Point out each malaria parasite.
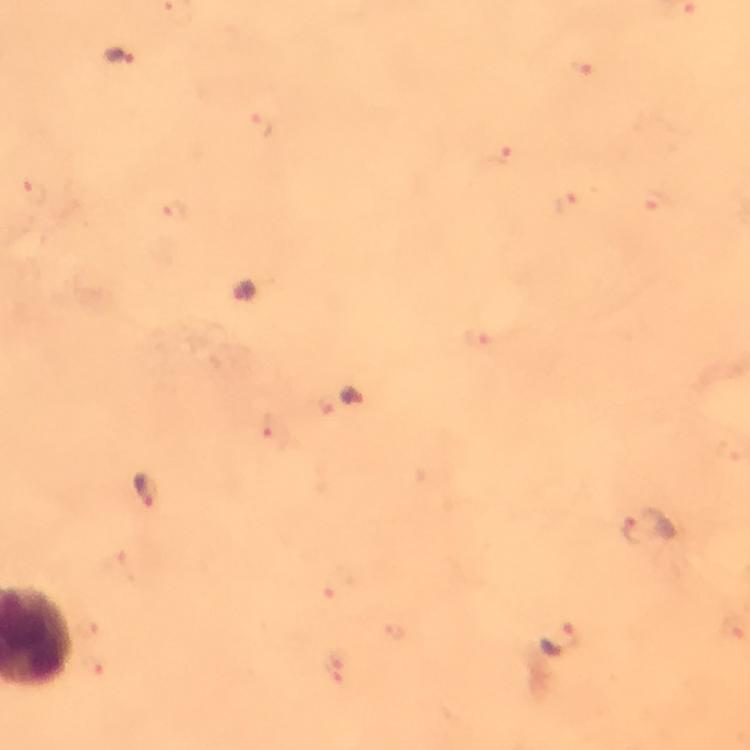

Approximate centers as (x, y) in pixels.
Malaria parasites: (119, 56), (242, 291), (352, 397), (143, 492), (650, 528), (562, 639).

immersion oil = applied
magnification = 100x
stain = Giemsa
capture = smartphone camera through the microscope
preparation = thick blood film
image size = 750×750 pixels
cropped from = one field of view
context = from a diagnostic examination for malaria